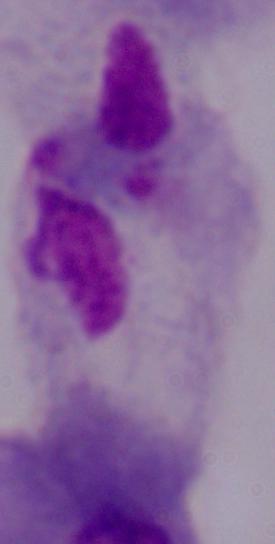

{
  "magnification": "1000x",
  "modality": "photomicrograph",
  "identification": "trichomonad"
}